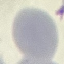
malaria status = uninfected
image type = automatically extracted cell patch, resized to 64 × 64 pixels
stain = Giemsa
preparation = thin blood film
capture = smartphone through the microscope eyepiece